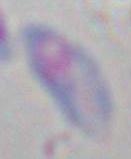

Summary:
  - Identification: Toxoplasma gondii
  - Magnification: 1000x
  - Modality: micrograph